Describe the morphology of the erythrocytes.
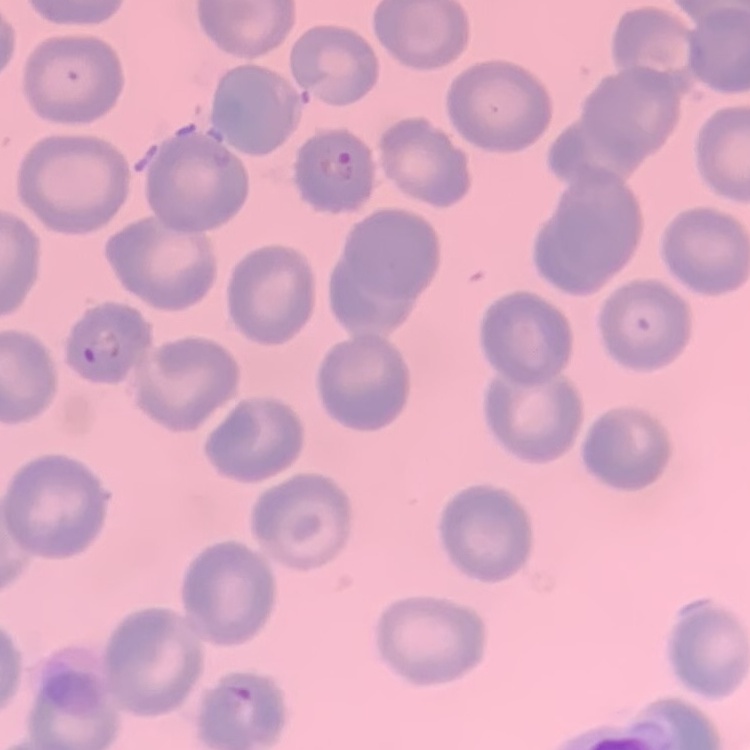
No rouleaux formation.

preparation: thin blood film
image_type: square crop of a larger photomicrograph
stain: Field's or Giemsa